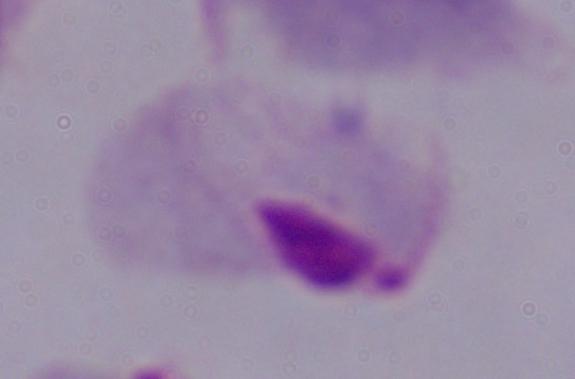

{
  "modality": "photomicrograph",
  "magnification": "1000x",
  "identification": "trichomonad"
}